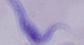

Summary:
  - Modality: micrograph
  - Magnification: 1000x
  - Identification: trypanosome